Point out each leukocyte.
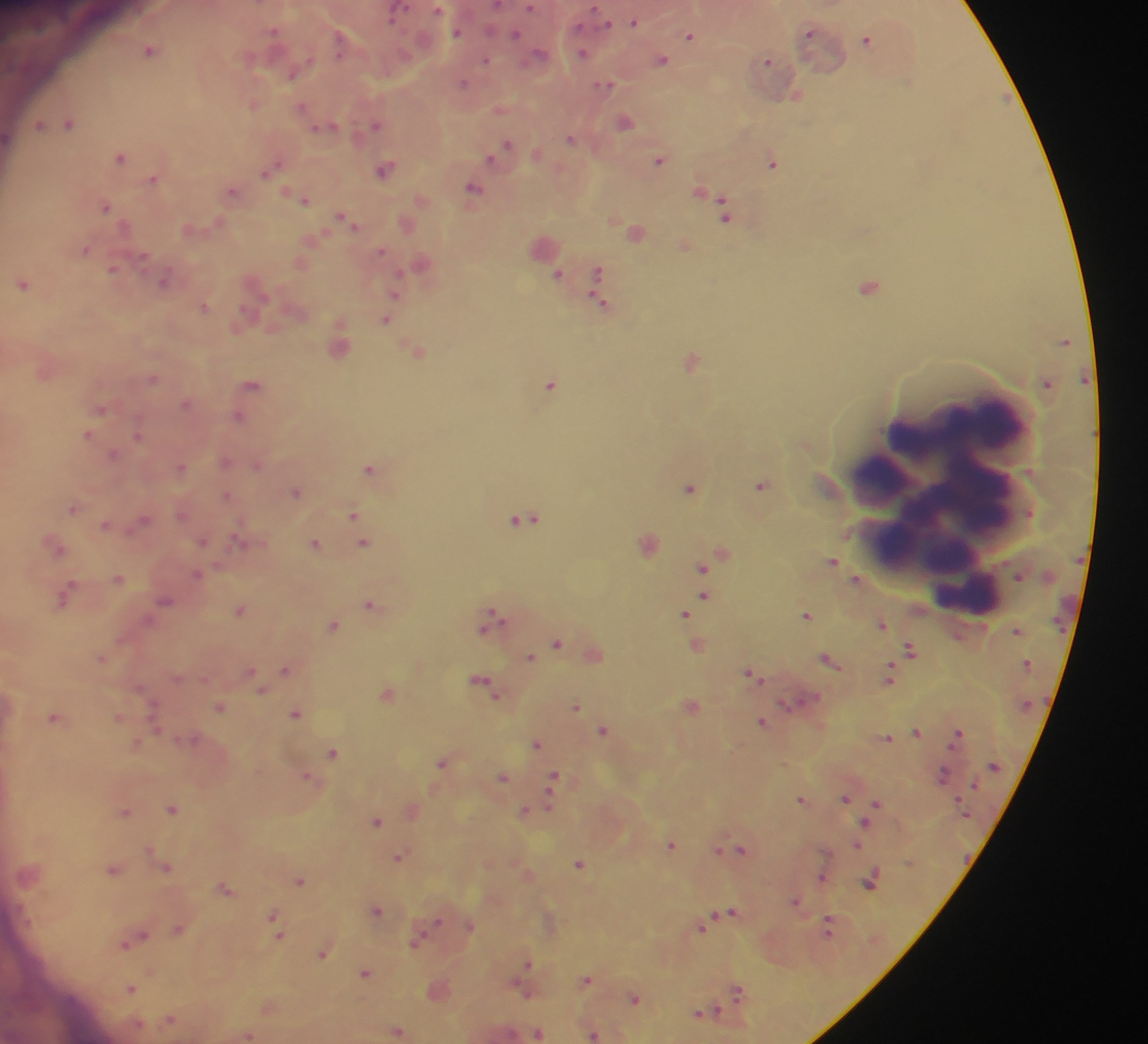

Approximate centers as x y in pixels.
Leukocytes: 946 507; 968 598.

Summary:
  - Plasmodium parasite locations: 530 7; 438 9; 395 15; 634 22; 607 24; 273 30; 810 32; 457 33; 515 34; 690 36; 867 39; 339 41; 150 49; 540 53; 583 53; 662 60; 486 61; 767 61; 292 75; 463 83; 605 84; 797 96; 302 108; 625 122; 69 123; 39 124; 375 125; 323 127; 570 138; 507 145; 120 157; 491 158; 660 160; 773 162; 268 170; 384 170; 153 179; 473 188; 232 191; 305 200; 106 206; 724 209; 346 219; 85 250; 382 251; 143 256; 112 269; 597 273; 558 274; 164 280; 23 283; 869 286; 397 291; 599 292; 204 306; 386 320; 693 361; 153 378; 252 384; 550 384; 186 404; 101 409; 239 417; 87 435; 138 435; 113 455; 226 461; 257 465; 181 467; 370 468; 761 486; 690 489; 296 491; 227 495; 73 508; 181 514; 353 514; 143 519; 523 519; 105 525; 202 542; 238 543; 314 543; 364 543; 55 548; 833 561; 702 568; 197 575; 119 579; 855 579; 66 595; 704 597; 166 601; 372 605; 240 611; 685 613; 806 615; 493 618; 882 624; 334 626; 557 643; 910 651; 529 657; 100 658; 829 660; 285 669; 250 672; 752 674; 888 675; 484 684; 139 689; 261 690; 786 704; 576 706; 220 707; 296 714; 53 718; 118 718; 763 721; 155 726; 602 730; 917 732; 958 733; 887 738; 191 739; 536 743; 136 744; 333 753; 441 763; 943 775; 308 777; 503 777; 552 783; 550 797; 845 798; 801 799; 876 803; 171 809; 125 811; 523 811; 377 821; 865 824; 671 844; 858 844; 718 849; 741 849; 149 850; 398 856; 579 864; 166 867; 113 870; 822 878; 299 880; 871 880; 225 888; 796 902; 377 911; 731 911; 273 918; 437 922; 470 927; 703 928; 829 928; 178 929; 278 931; 143 935; 416 941; 125 943; 323 953; 528 962; 365 972; 151 973; 587 980; 130 989; 521 990; 738 991; 635 999; 713 1010; 700 1013; 171 1019; 397 1031; 538 1034; 593 1035
  - Country: Ghana
  - Capture: mobile-phone photograph through a microscope
  - Field of view: single
  - Preparation: thick blood smear
  - Image size: 1148×1044 pixels